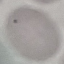

Malaria status: uninfected. Cell patch, automatically extracted from a larger field of view and resized to 64 × 64 pixels. Photographed with a smartphone camera at the microscope eyepiece. Giemsa-stained preparation. Thin blood smear.